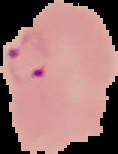
{
  "preparation": "thin blood film",
  "result": "malaria parasites identified",
  "image_type": "segmented cell region on a black background",
  "image_size": "118×154 pixels"
}